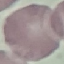
Summary:
  - Malaria status: uninfected
  - Preparation: thin smear
  - Capture: smartphone through the microscope eyepiece
  - Stain: Giemsa
  - Image type: cell patch, automatically extracted from a larger field of view and resized to 64 × 64 pixels